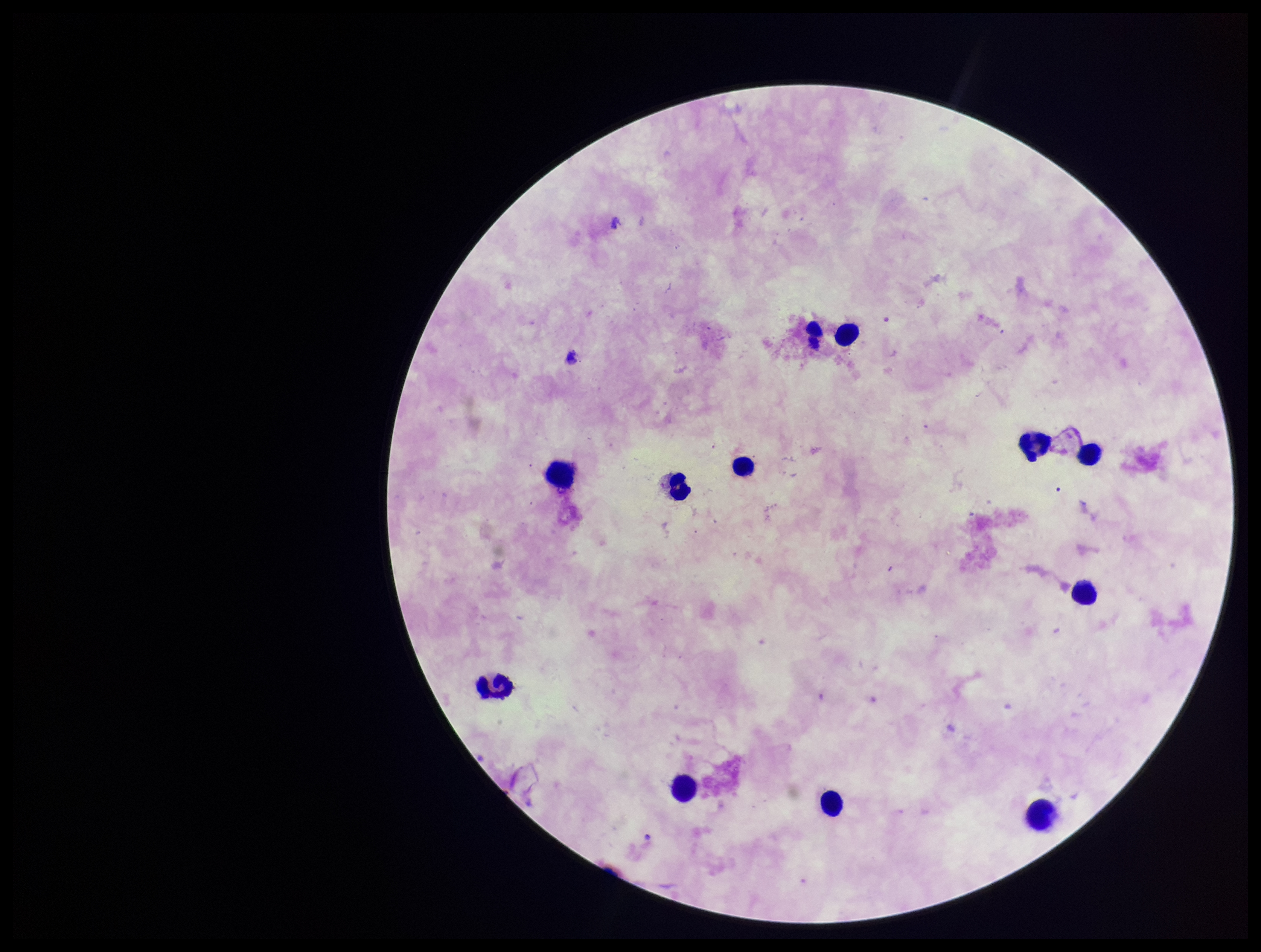

field of view = single
leukocyte count = 12
image size = 1261×952 pixels
parasite count = 0
patient malaria status = negative
capture = smartphone photograph through the microscope eyepiece
Plasmodium parasites = none seen
preparation = thick smear
stain = Giemsa